Locate every Plasmodium falciparum-infected red blood cell.
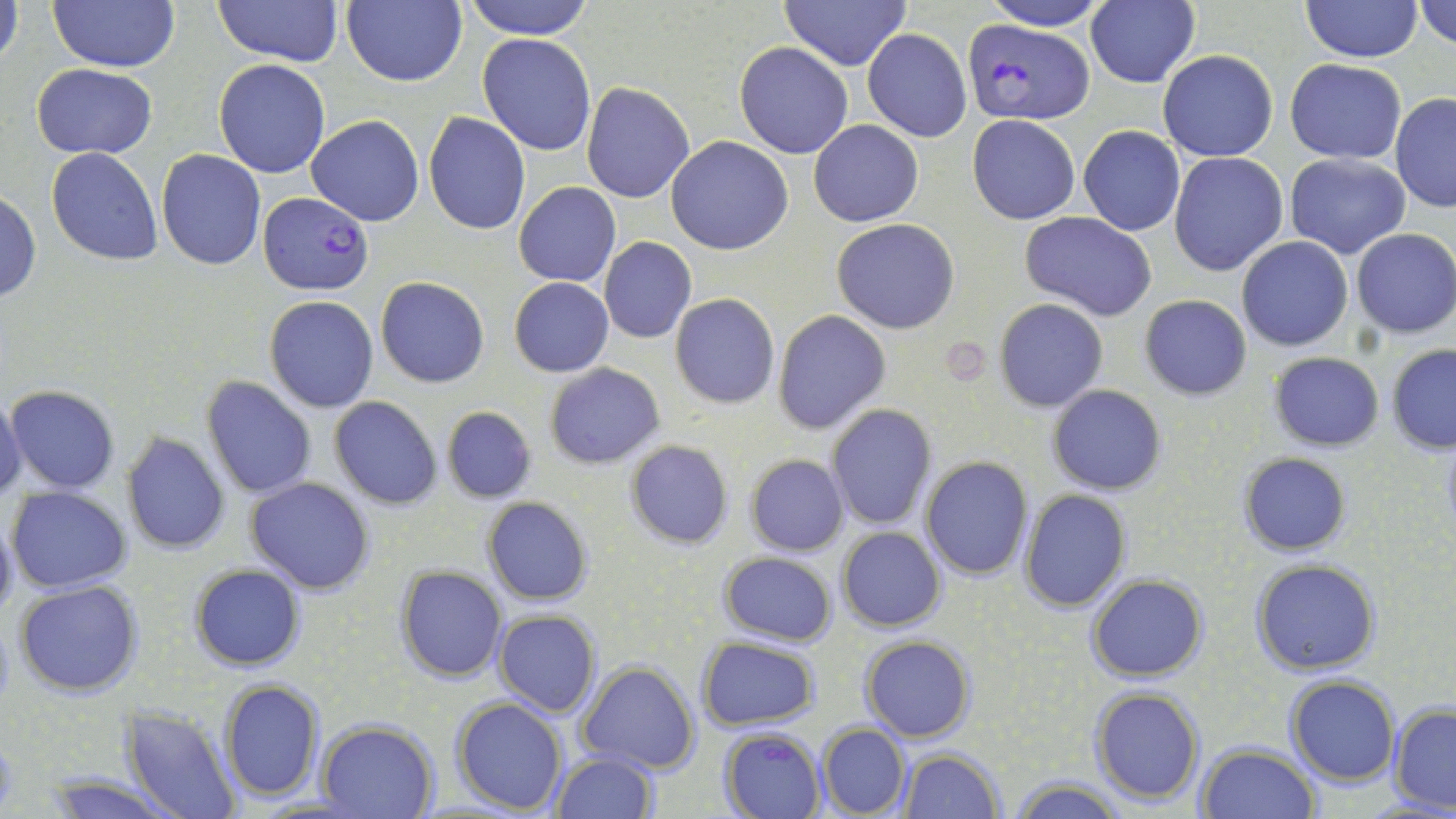

Approximate bounding boxes as (x1,y1)-(x2,y2) corner pairs in pixels.
Plasmodium falciparum-infected red blood cells: (963,20)-(1094,124), (257,192)-(374,296), (721,727)-(827,819).

Uninfected red blood cell locations: (0,0)-(24,76), (50,0)-(181,73), (217,0)-(343,66), (343,0)-(467,88), (464,0)-(596,40), (782,0)-(910,70), (977,0)-(1112,30), (1301,0)-(1423,62), (1415,1)-(1455,51), (1086,2)-(1200,88), (862,29)-(972,144), (478,35)-(597,156), (734,42)-(854,159), (1157,49)-(1278,161), (214,59)-(330,178), (1284,59)-(1406,163), (31,63)-(157,159), (581,82)-(697,203), (1391,93)-(1456,212), (423,112)-(531,235), (967,114)-(1080,224), (306,115)-(425,226), (810,120)-(924,226), (1078,126)-(1185,236), (667,135)-(793,255), (46,148)-(163,264), (156,149)-(266,271), (1284,151)-(1411,259), (1169,152)-(1289,275), (514,182)-(620,287), (1,192)-(42,303), (1020,212)-(1157,320), (832,219)-(960,334), (1351,228)-(1456,339), (598,237)-(696,343), (1236,237)-(1354,351), (375,276)-(489,388), (509,276)-(614,376), (670,293)-(779,408), (1138,294)-(1252,400), (264,296)-(379,412), (993,299)-(1108,412), (773,309)-(891,434), (1387,344)-(1456,454), (1268,352)-(1384,451), (544,363)-(665,468), (203,375)-(317,499), (1048,384)-(1166,495), (5,385)-(120,495), (0,395)-(26,505), (329,397)-(443,509), (826,405)-(935,530), (441,406)-(538,504), (122,432)-(230,555), (624,440)-(733,550), (1238,453)-(1351,557), (745,454)-(848,557), (920,456)-(1033,579), (246,476)-(376,595), (6,486)-(132,592), (1018,489)-(1133,611), (482,497)-(592,605), (0,512)-(18,625), (836,526)-(946,631), (718,551)-(837,646), (1250,559)-(1382,676), (189,563)-(304,672), (395,566)-(506,682), (1086,573)-(1208,681), (14,581)-(144,698), (492,609)-(602,717), (861,635)-(975,741), (696,637)-(821,732), (579,661)-(700,774), (1285,677)-(1400,786), (220,678)-(325,802), (1089,686)-(1205,805), (450,696)-(568,814), (1389,705)-(1456,813), (121,709)-(242,819), (316,720)-(438,819), (818,723)-(910,817), (1196,743)-(1318,819), (898,747)-(1006,818), (550,752)-(658,819), (35,773)-(184,819), (1008,777)-(1127,818). Platelet locations: (946,341)-(988,382). Slide-level diagnosis: Plasmodium falciparum. Single field of view. Captured at 1000x magnification. Light microscopy. Image is 1456×819 pixels. May-Grünwald-Giemsa-stained preparation. Thin blood film.